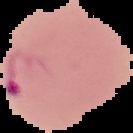
Summary:
  - Image size: 133×133 pixels
  - Malaria status: parasitized
  - Preparation: thin blood film
  - Image type: cell region segmented out of the field of view; surrounding area masked to black